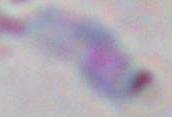

{
  "magnification": "1000x",
  "identification": "Toxoplasma gondii",
  "modality": "photomicrograph"
}